Describe the morphology of the erythrocytes.
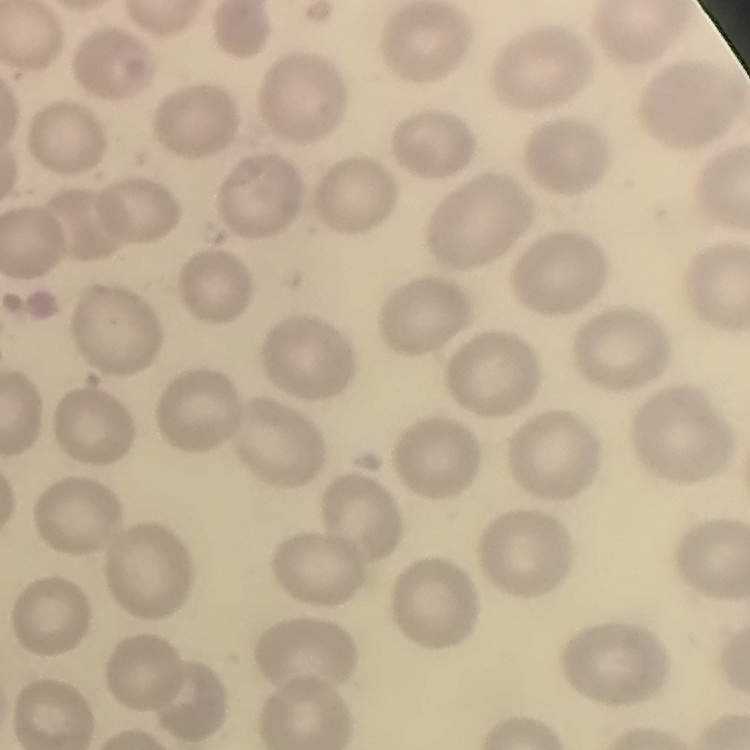
No rouleaux formation.

stain = Field's or Giemsa
image type = square crop of a larger photomicrograph
preparation = thin blood smear